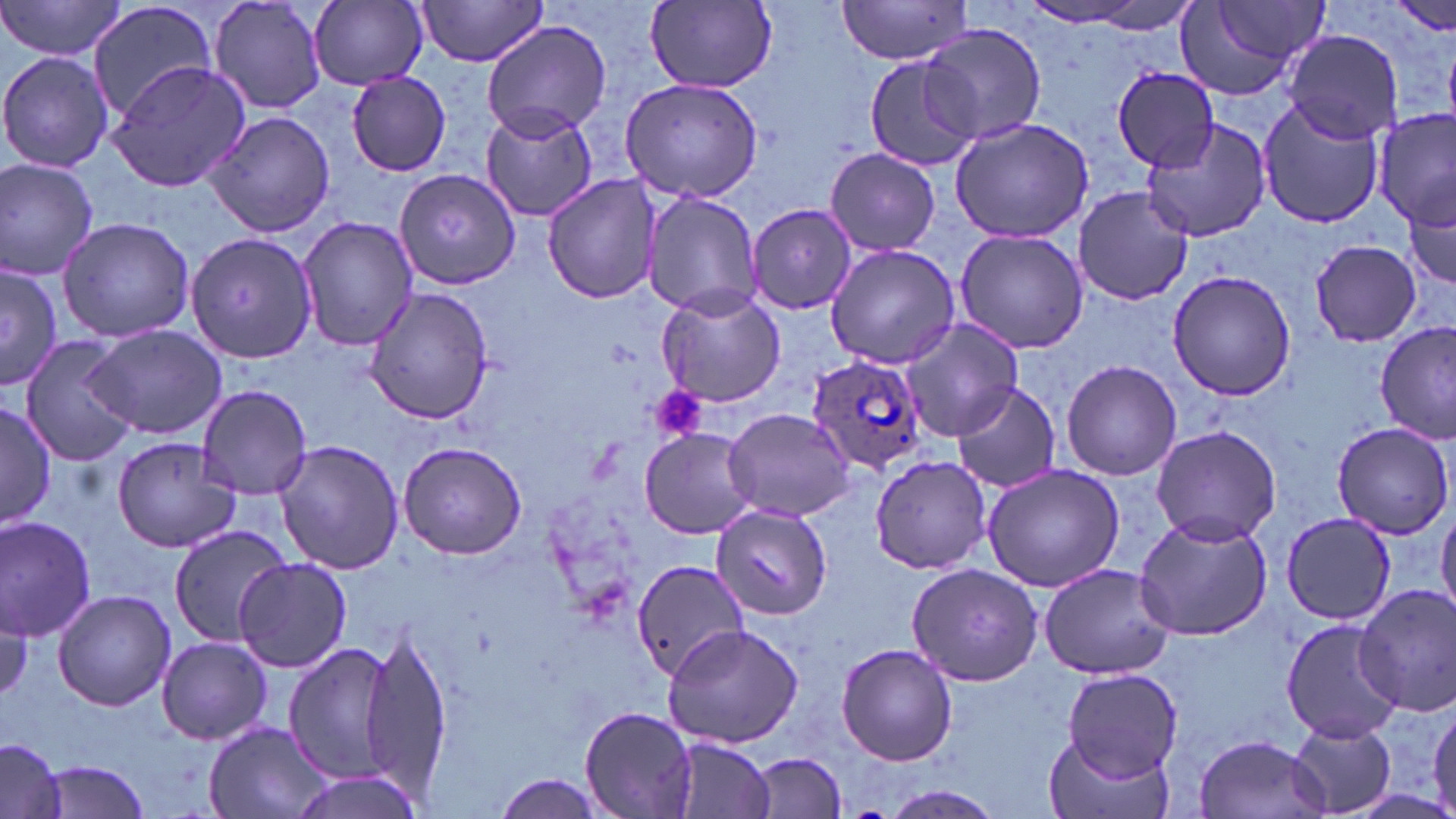 Approximate bounding boxes as (x1,y1)-(x2,y2) corner pairs in pixels. Uninfected red blood cell locations: (0,0)-(129,63), (207,0)-(329,115), (85,1)-(222,123), (309,1)-(427,88), (413,1)-(553,68), (647,1)-(778,90), (833,1)-(975,65), (1178,1)-(1327,98), (1014,3)-(1159,28), (480,19)-(611,140), (921,25)-(1047,146), (1283,30)-(1401,142), (0,50)-(115,174), (862,53)-(985,171), (104,60)-(252,193), (1112,68)-(1221,172), (345,69)-(452,175), (619,77)-(767,205), (1256,100)-(1387,229), (479,105)-(598,223), (1374,108)-(1455,234), (200,109)-(336,239), (949,115)-(1095,244), (1140,120)-(1274,244), (824,148)-(941,256), (0,157)-(100,280), (393,170)-(519,287), (542,173)-(663,305), (1405,185)-(1455,300), (1073,186)-(1192,306), (640,190)-(764,318), (749,203)-(859,314), (58,214)-(195,344), (296,214)-(417,349), (954,228)-(1089,354), (185,232)-(319,364), (1306,238)-(1424,348), (825,243)-(964,368), (0,264)-(62,389), (1166,269)-(1296,401), (364,285)-(494,422), (656,287)-(786,407), (896,316)-(1024,442), (1374,323)-(1454,443), (84,324)-(228,441), (20,336)-(142,465), (1062,358)-(1181,481), (948,381)-(1063,496), (194,385)-(315,498), (0,396)-(57,531), (723,407)-(856,523), (1331,423)-(1453,538), (1149,425)-(1281,546), (638,428)-(757,538), (111,434)-(242,553), (274,439)-(406,576), (397,439)-(526,561), (869,453)-(994,574), (981,462)-(1128,592), (711,506)-(832,619), (1436,507)-(1456,621), (1280,512)-(1395,626), (0,514)-(99,641), (1132,514)-(1274,642), (166,526)-(295,644), (235,558)-(351,673), (628,558)-(747,682), (905,561)-(1047,685), (1037,562)-(1175,679), (1352,583)-(1456,718), (53,590)-(176,711), (1282,617)-(1399,742), (662,624)-(806,748), (359,627)-(453,802), (155,635)-(272,746), (281,640)-(400,785), (836,642)-(958,767), (1062,668)-(1182,780), (1428,700)-(1456,816), (579,704)-(700,817), (1286,718)-(1397,816), (202,721)-(334,819), (1041,730)-(1170,819), (1192,733)-(1331,819), (669,736)-(777,819), (0,740)-(67,819), (751,752)-(846,816), (34,759)-(154,817), (285,769)-(426,818), (490,775)-(613,818), (877,787)-(1006,819). Plasmodium ovale-infected red blood cell locations: (808,357)-(926,477). Platelet locations: (649,386)-(707,445). Slide-level diagnosis: Plasmodium ovale. One field of a larger specimen. Image is 1456×819 pixels. May-Grünwald-Giemsa-stained preparation. Thin blood smear. Light microscopy. 1000x magnification.